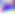
Photomicrograph. Toxoplasma gondii is shown. 400x magnification.